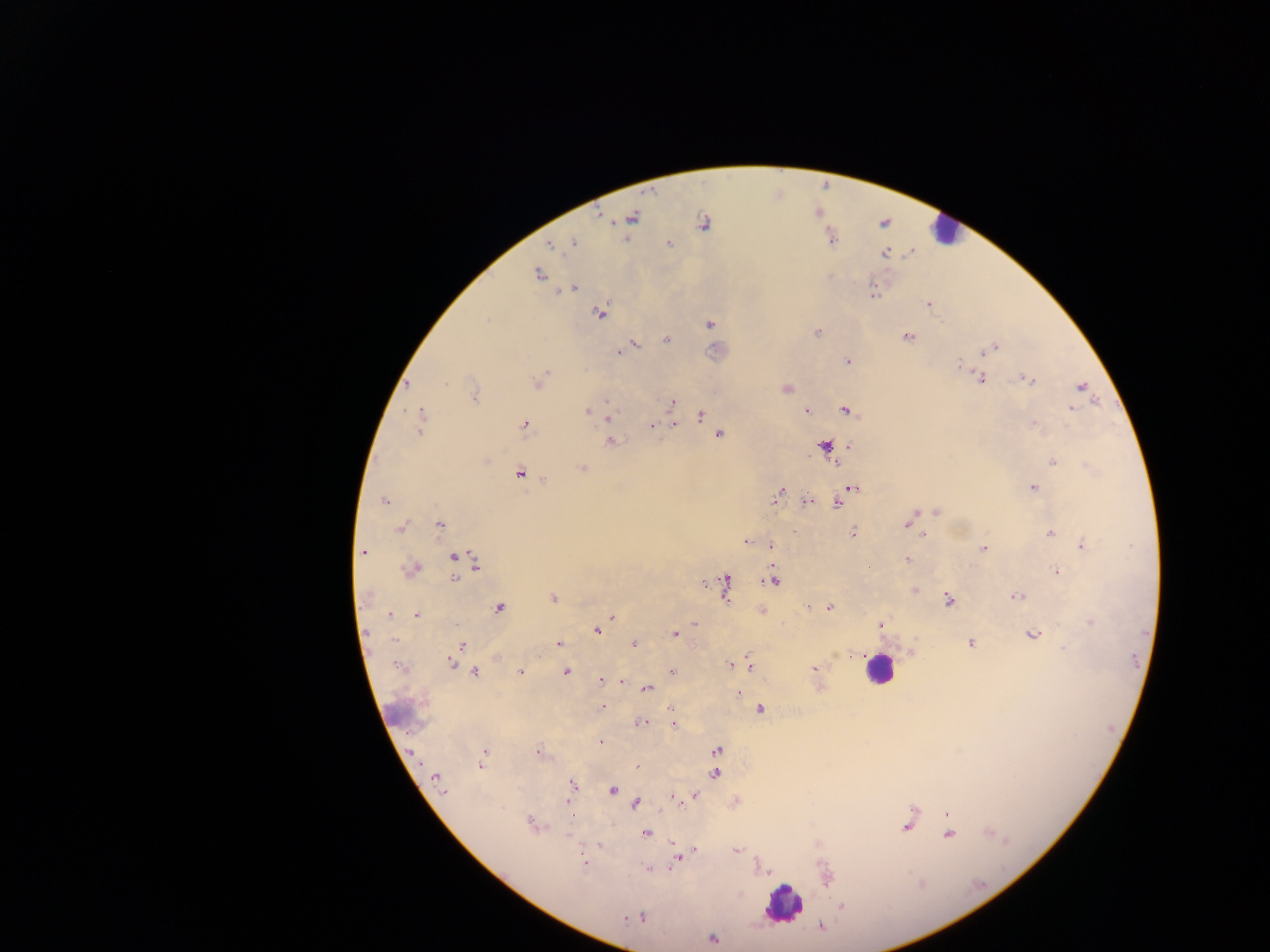

Approximate centers as [x, y] in pixels. Leukocyte locations: [946, 229], [878, 669], [782, 902]. Plasmodium parasite locations: [599, 216], [630, 217], [703, 223], [884, 223], [830, 236], [572, 242], [668, 243], [550, 244], [885, 253], [539, 273], [572, 288], [873, 295], [928, 304], [599, 313], [709, 323], [818, 332], [907, 337], [666, 340], [633, 344], [994, 347], [625, 349], [618, 353], [847, 360], [980, 378], [1026, 378], [537, 383], [406, 384], [1081, 386], [786, 388], [474, 393], [670, 402], [1071, 408], [845, 409], [587, 411], [805, 411], [701, 415], [607, 418], [420, 422], [674, 423], [662, 424], [1034, 424], [524, 425], [652, 425], [719, 433], [609, 441], [848, 445], [824, 446], [1052, 461], [1087, 465], [582, 468], [519, 473], [1032, 486], [852, 488], [776, 495], [843, 499], [384, 500], [806, 501], [837, 501], [936, 510], [909, 519], [438, 525], [401, 527], [1049, 532], [852, 533], [923, 535], [746, 541], [770, 545], [1082, 545], [983, 548], [362, 551], [454, 556], [463, 560], [907, 560], [475, 563], [411, 569], [1055, 570], [455, 577], [774, 579], [724, 584], [915, 591], [1016, 596], [552, 598], [948, 600], [498, 606], [807, 607], [829, 607], [762, 610], [390, 614], [415, 614], [612, 617], [1090, 621], [695, 623], [880, 624], [596, 630], [675, 634], [1033, 635], [633, 643], [971, 643], [558, 644], [461, 645], [911, 652], [495, 656], [450, 662], [731, 664], [737, 664], [749, 664], [400, 667], [815, 669], [566, 670], [521, 671], [671, 671], [475, 672], [817, 673], [601, 680], [620, 681], [819, 687], [646, 688], [736, 692], [601, 707], [759, 708], [640, 722], [673, 723], [600, 742], [716, 750], [484, 751], [539, 752], [482, 766], [636, 766], [714, 773], [436, 778], [439, 786], [571, 786], [612, 790], [569, 794], [695, 795], [672, 797], [635, 802], [735, 802], [947, 813], [532, 825], [907, 827], [645, 833], [948, 834], [674, 844], [599, 845], [693, 850], [734, 850], [677, 857], [583, 860], [647, 868], [841, 907], [634, 917], [626, 918], [641, 918], [820, 925], [711, 939]. Thick blood film. One field of view. Sample from Ghana. Photographed through a microscope with a mobile-phone camera. Image is 1270×952 pixels.